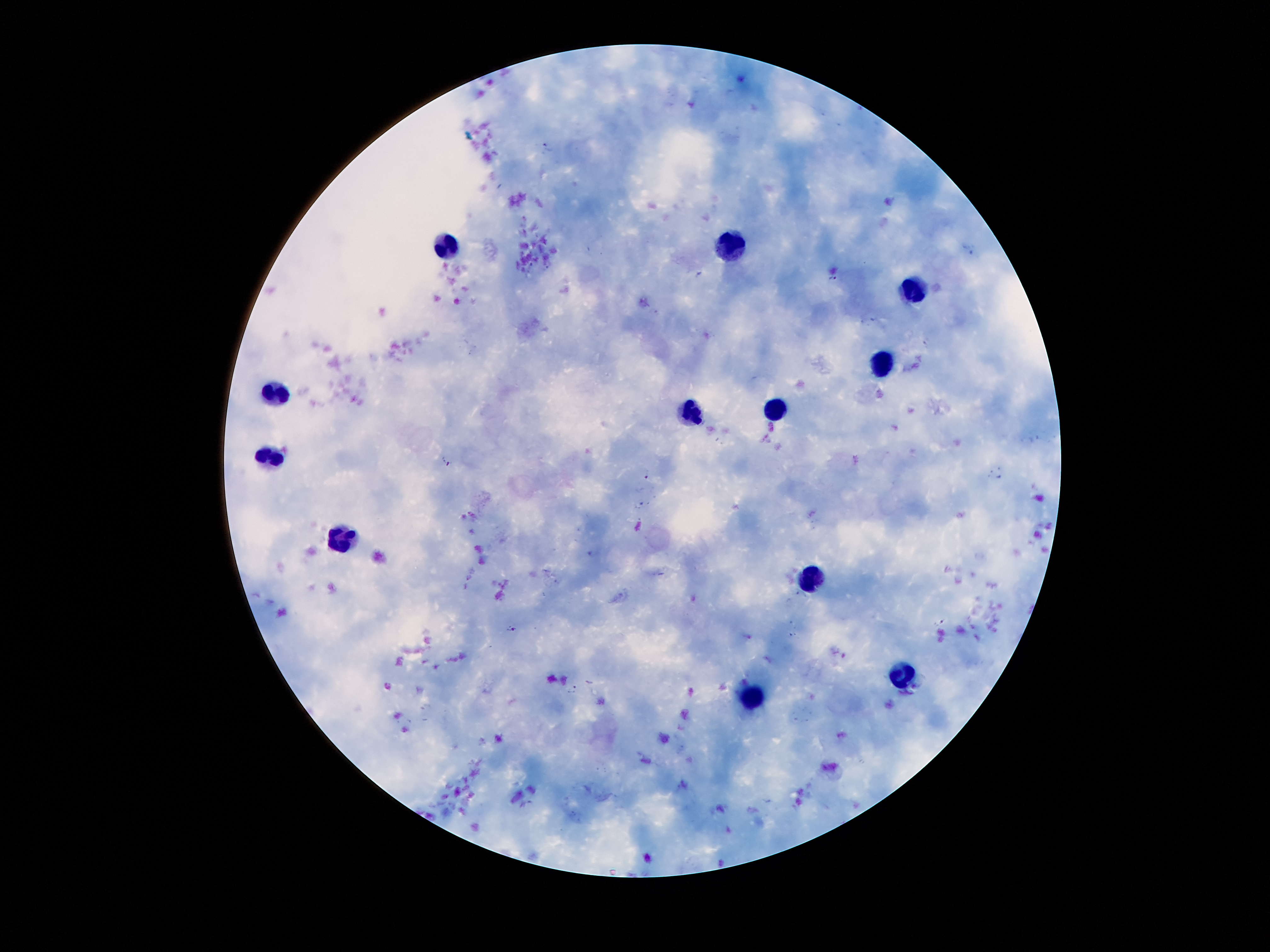
Approximate centers as (x, y) in pixels. Leukocyte locations: (445, 246), (728, 247), (920, 294), (885, 363), (275, 392), (775, 406), (692, 411), (274, 456), (347, 536), (803, 577), (899, 677), (743, 697). Plasmodium parasite locations: (970, 248), (699, 275), (832, 278), (448, 461), (648, 475), (941, 621), (514, 630), (573, 688). Thick peripheral-blood smear. Single field of view. Patient malaria status: positive for Plasmodium falciparum. 100x magnification. Photographed through the microscope eyepiece with a smartphone camera. Image is 1270×952 pixels. Giemsa stain.